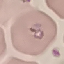
{
  "result": "malaria parasites detected",
  "capture": "smartphone camera at the microscope eyepiece",
  "preparation": "thin smear",
  "image_type": "cell patch, automatically extracted from a larger field of view and resized to 64 × 64 pixels",
  "stain": "Giemsa"
}